Classify this cell by malaria status.
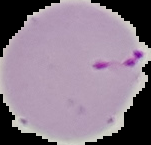

It is parasitized.

image type = cell region segmented out of the field of view; surrounding area masked to black
preparation = thin blood smear
image size = 151×145 pixels